Identify the parasite.
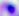
Toxoplasma gondii.

Captured at 400x magnification. Micrograph.